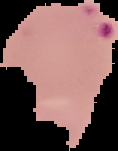

Summary:
  - Image type: segmented cell region with the area outside set to black
  - Image size: 118×151 pixels
  - Preparation: thin blood film
  - Malaria status: parasitized